Classify this cell by malaria status.
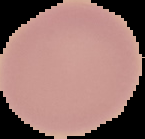

Uninfected.

preparation: thin blood film
image_size: 145×139 pixels
image_type: segmented cell region with the area outside set to black